Report the malaria status of this cell.
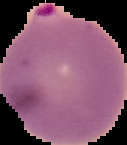
Parasitized.

image type = segmented cell region on a black background
preparation = thin blood smear
image size = 127×145 pixels